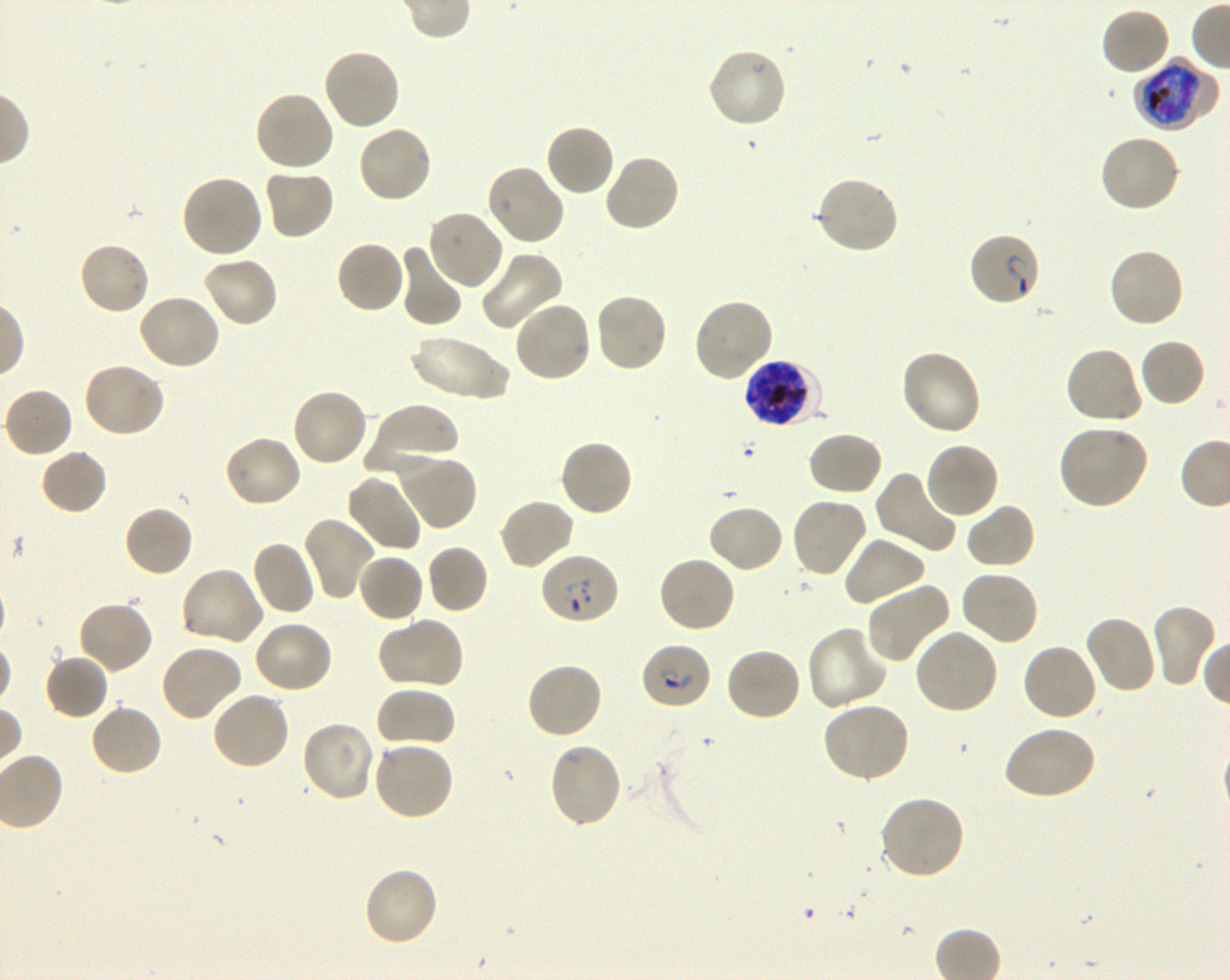

Not every red blood cell is marked. A life-cycle stage — or a range of stages, where the recorded stages span more than one — follows each staged infected red blood cell.
locations_of_infected_red_blood_cells: 'approximate bounding boxes as (x1, y1, x2, y2) in pixels: (1134, 57, 1217, 131) late trophozoite to late schizont; (968, 232, 1042, 308) ring; (743, 359, 821, 429) late trophozoite to late schizont; (539, 552, 620, 625) ring; (640, 640, 711, 709) ring'
objective: 100x, oil immersion, numerical aperture 1.30
preparation: thin blood film
culture: shaking in-vitro Plasmodium falciparum strain 3D7
donor_blood_group: O+
locations_of_uninfected_red_blood_cells: 'approximate bounding boxes as (x1, y1, x2, y2) in pixels: (1100, 7, 1171, 77), (321, 47, 401, 131), (706, 47, 788, 129), (253, 90, 336, 173), (544, 123, 616, 198), (357, 124, 434, 203), (1098, 133, 1183, 213), (603, 152, 682, 234), (485, 164, 565, 247), (262, 166, 335, 241), (180, 174, 263, 259), (814, 176, 899, 256), (425, 208, 505, 291), (334, 240, 406, 314), (78, 241, 151, 316), (397, 245, 462, 328), (480, 248, 564, 331), (1107, 248, 1185, 329), (201, 254, 279, 329), (594, 292, 670, 374), (135, 293, 221, 372), (692, 296, 774, 382), (513, 300, 593, 383), (409, 336, 512, 402), (1138, 338, 1206, 409), (1063, 346, 1143, 427), (898, 349, 982, 436), (81, 361, 165, 439), (3, 387, 73, 459), (289, 387, 368, 468), (365, 403, 459, 476), (1056, 423, 1150, 510), (806, 431, 884, 497), (223, 435, 303, 509), (558, 438, 634, 518), (924, 441, 1000, 520), (39, 448, 108, 516), (393, 452, 478, 532), (875, 470, 960, 556), (345, 473, 422, 553), (497, 496, 575, 571), (790, 496, 868, 578), (965, 502, 1037, 570), (707, 504, 785, 574), (123, 505, 194, 579), (300, 515, 374, 600), (843, 534, 927, 608), (251, 540, 316, 616), (425, 544, 489, 614), (356, 553, 425, 623), (657, 554, 737, 634), (179, 566, 265, 646), (958, 570, 1040, 647), (865, 580, 952, 664), (76, 600, 154, 675), (1150, 603, 1217, 688), (1083, 614, 1158, 695), (378, 617, 465, 690), (251, 621, 334, 695), (805, 626, 887, 712), (912, 628, 999, 716), (1021, 642, 1099, 722), (158, 643, 243, 722), (724, 646, 802, 723), (44, 652, 110, 721), (524, 660, 604, 740), (374, 685, 456, 749), (211, 690, 291, 771), (820, 701, 910, 783), (89, 703, 163, 777), (300, 719, 379, 803), (1003, 724, 1097, 801), (371, 739, 455, 822), (547, 741, 622, 829), (878, 794, 966, 880), (362, 865, 440, 947)'
stain: Giemsa
field_of_view: one from this slide
image_size: 1230×980 pixels